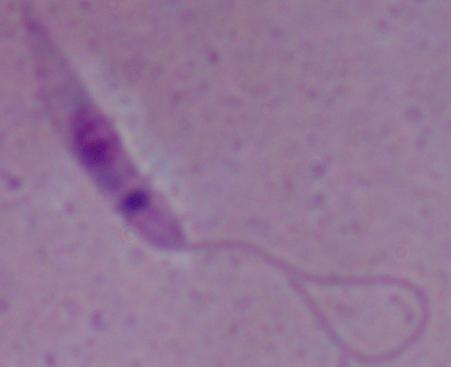
modality: micrograph
magnification: 1000x
identification: Leishmania